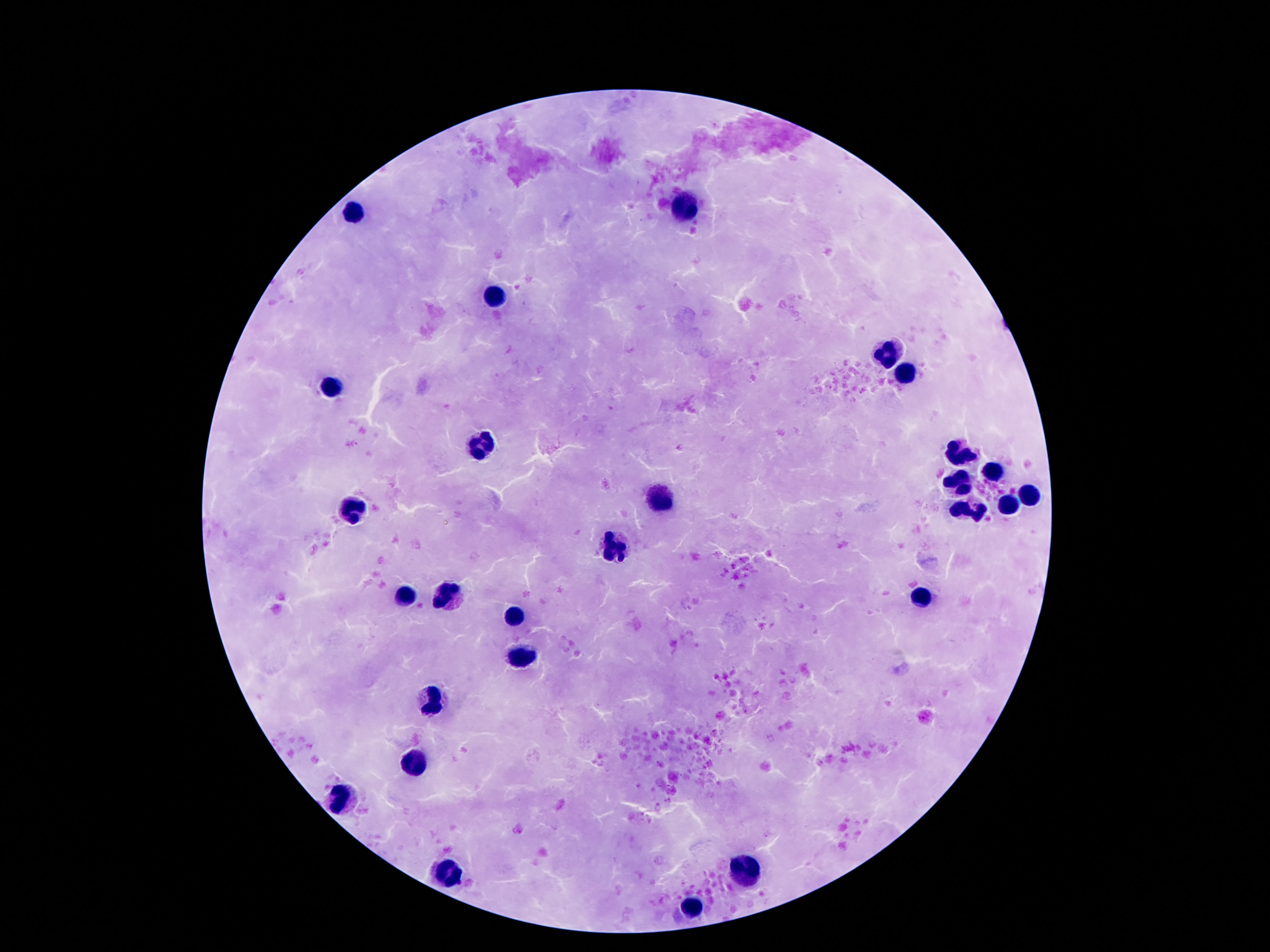
Approximate centers as {x, y} in pixels. Leukocyte locations: {683, 208}, {351, 211}, {498, 296}, {888, 355}, {905, 376}, {332, 387}, {485, 445}, {957, 452}, {991, 472}, {959, 484}, {1028, 495}, {655, 500}, {1006, 506}, {353, 510}, {970, 513}, {618, 547}, {405, 594}, {448, 594}, {920, 599}, {513, 615}, {524, 657}, {433, 698}, {416, 759}, {340, 800}, {442, 873}, {741, 876}, {689, 909}. Thick peripheral-blood smear. 100x magnification. Photographed through the microscope eyepiece with a smartphone camera. Patient malaria status: uninfected. Giemsa-stained preparation. One field from this slide. Image is 1270×952 pixels.